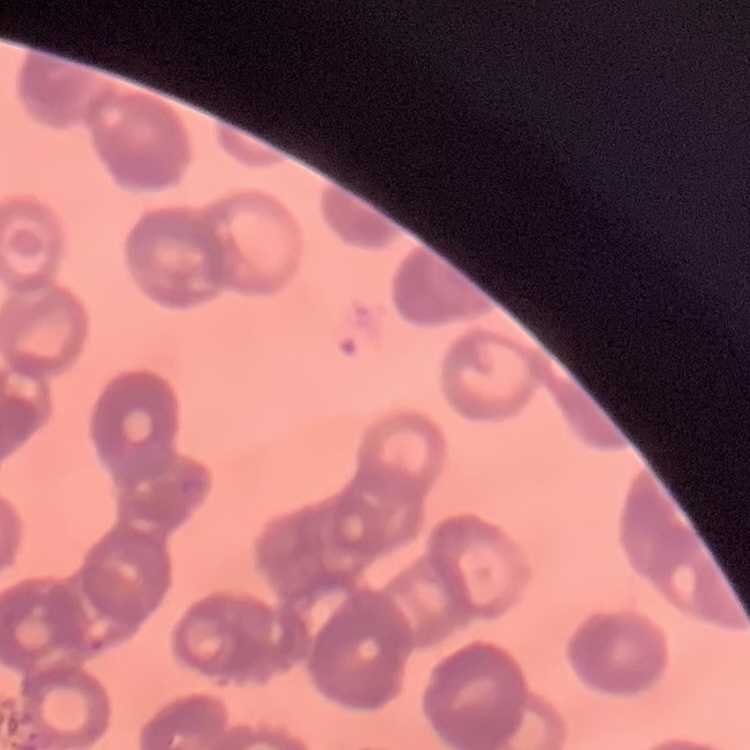

{
  "red_blood_cell_morphology": "rouleaux formation",
  "image_type": "one tile cut from a larger photomicrograph",
  "stain": "Field's or Giemsa",
  "preparation": "thin blood smear"
}